Point out each malaria parasite.
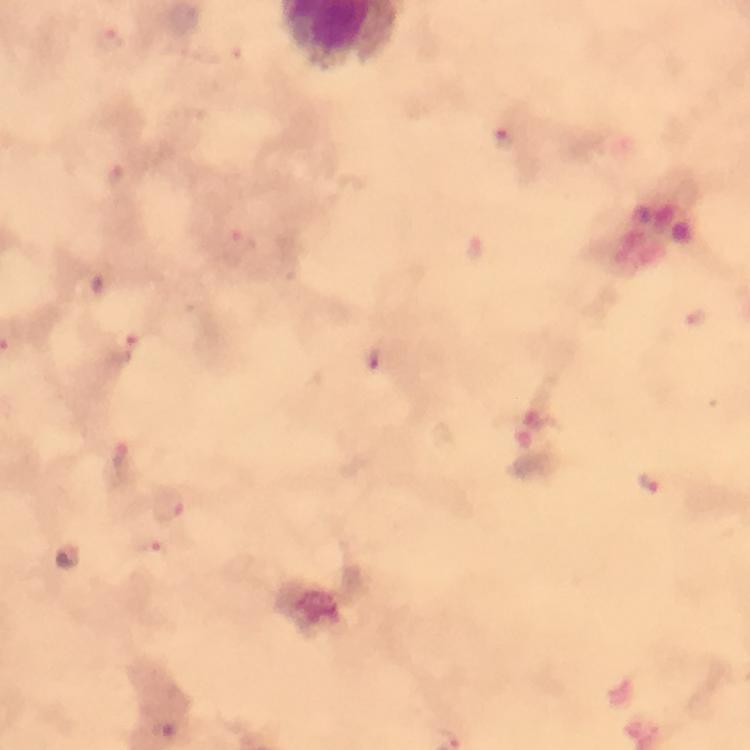
Approximate centers as (x, y) in pixels.
Malaria parasites: (110, 39), (502, 140), (113, 174), (245, 243), (474, 246), (128, 348), (376, 359), (121, 459), (652, 484), (168, 505), (156, 550), (163, 732), (451, 734).

Photographed through the microscope with a smartphone camera. Image is 750×750 pixels. 100x magnification. Cropped region of a single field of view. From a malaria diagnostic workup. Thick smear. Immersion oil was used. Giemsa-stained preparation.